Identify the parasite.
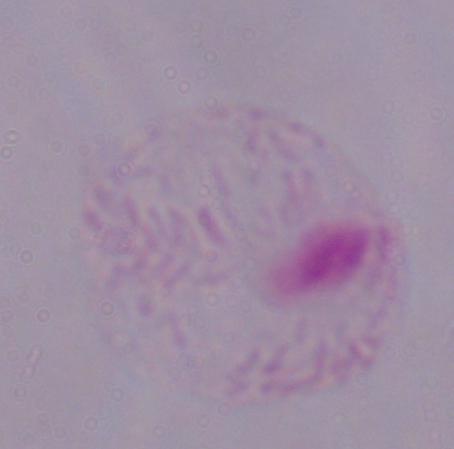

This is a trichomonad.

{
  "magnification": "1000x",
  "modality": "micrograph"
}